Name the parasite shown.
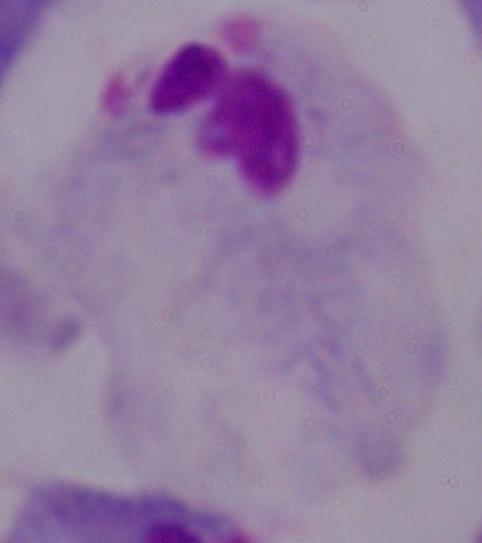
A trichomonad.

Summary:
  - Modality: photomicrograph
  - Magnification: 1000x